Name the parasite shown.
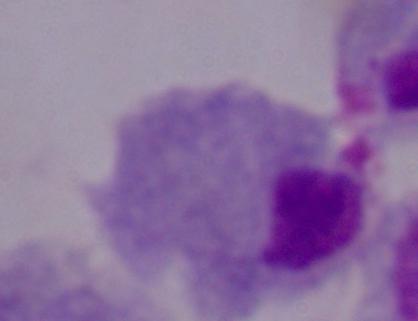
This is a trichomonad.

Photomicrograph. Captured at 1000x magnification.